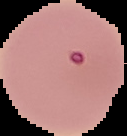

{
  "image_type": "segmented cell region with the area outside set to black",
  "image_size": "127×136 pixels",
  "preparation": "thin blood film",
  "result": "malaria parasites detected"
}